Report the malaria status of this cell.
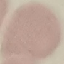
Uninfected.

Thin blood film. Acquired by smartphone through the microscope eyepiece. Automatically extracted cell patch, resized to 64 × 64 pixels. Giemsa stain.